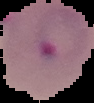

Summary:
  - Preparation: thin blood film
  - Image size: 94×103 pixels
  - Image type: segmented cell region with the area outside set to black
  - Malaria status: parasitized